Identify the blood parasite species.
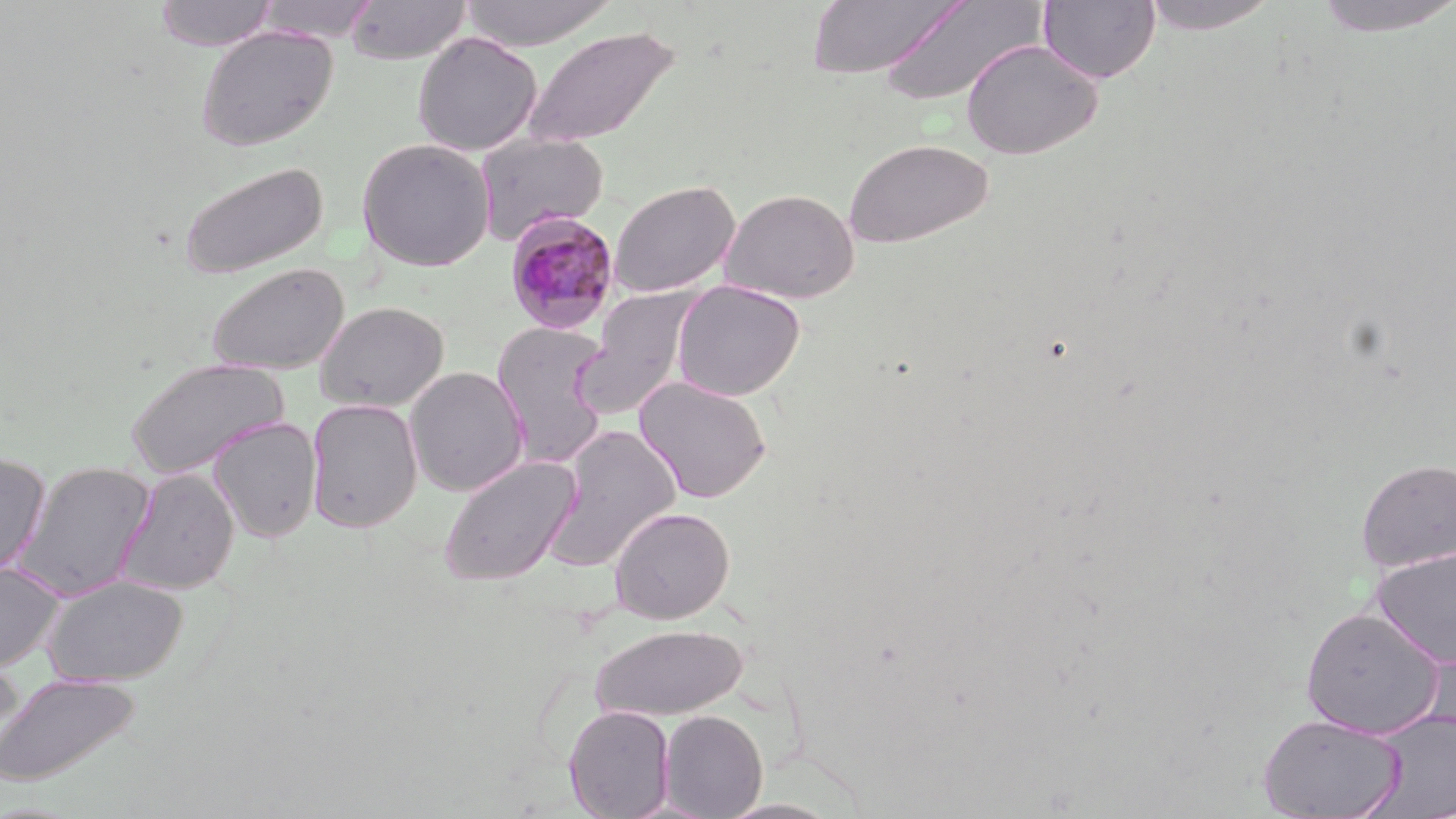
Plasmodium malariae.

{
  "field_of_view": "one of a larger specimen",
  "modality": "light microscopy",
  "preparation": "thin blood smear",
  "plasmodium_malariae_infected_red_blood_cell_locations": "approximate bounding boxes as (x1, y1, x2, y2) in pixels: (505, 211, 621, 334)",
  "stain": "May-Grünwald-Giemsa",
  "image_size": "1456×819 pixels",
  "magnification": "1000x",
  "uninfected_red_blood_cell_locations": "approximate bounding boxes as (x1, y1, x2, y2) in pixels: (153, 0, 279, 52), (345, 0, 471, 64), (457, 0, 617, 50), (877, 0, 1046, 107), (1139, 0, 1281, 35), (1310, 0, 1456, 39), (254, 1, 384, 42), (806, 1, 963, 80), (1037, 1, 1162, 84), (521, 24, 680, 150), (194, 26, 337, 152), (412, 32, 542, 155), (961, 39, 1104, 160), (475, 132, 608, 244), (356, 137, 495, 272), (843, 137, 994, 249), (175, 160, 328, 280), (609, 180, 740, 298), (720, 188, 860, 304), (205, 262, 349, 375), (672, 280, 806, 401), (574, 288, 699, 421), (315, 301, 448, 412), (491, 319, 611, 467), (124, 357, 290, 480), (405, 366, 528, 496), (634, 376, 772, 503), (306, 398, 423, 533), (209, 417, 323, 542), (543, 424, 681, 573), (0, 452, 51, 577), (438, 454, 582, 586), (1356, 458, 1456, 573), (13, 461, 156, 601), (116, 467, 239, 595), (609, 506, 735, 623), (1370, 548, 1456, 667), (0, 563, 65, 671), (43, 575, 188, 686), (1299, 606, 1445, 738), (590, 623, 748, 720), (0, 657, 27, 769), (0, 672, 140, 787), (563, 705, 675, 819), (659, 709, 767, 818), (1359, 709, 1456, 819), (1257, 713, 1406, 818)"
}